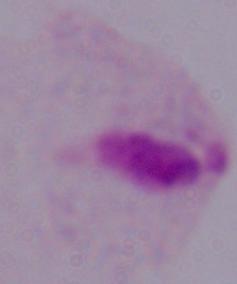
A trichomonad is seen. 1000x magnification. Micrograph.